Comment on the morphology of the erythrocytes.
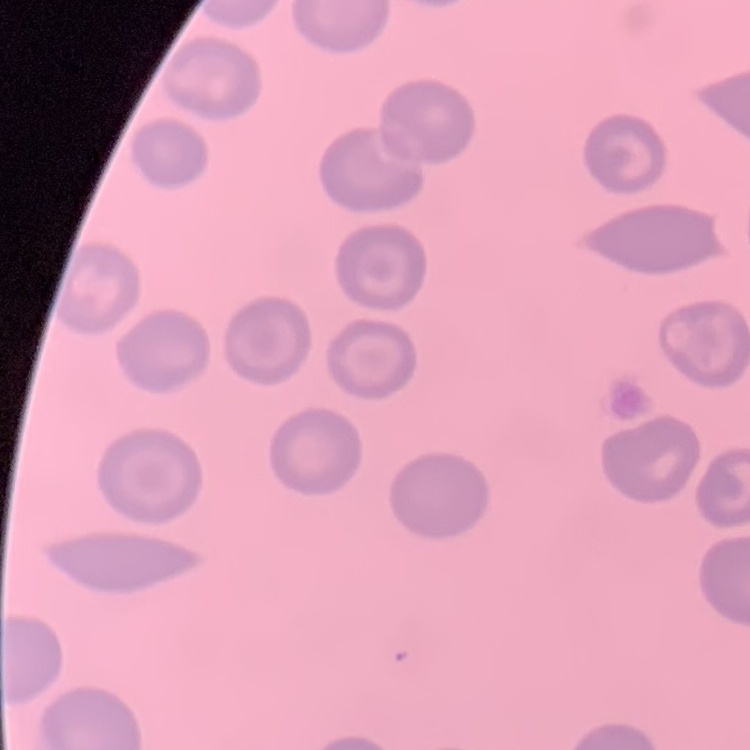

They show no rouleaux formation.

Field's or Giemsa stain. One tile cut from a larger photomicrograph. Thin blood smear.